Comment on the morphology of the erythrocytes.
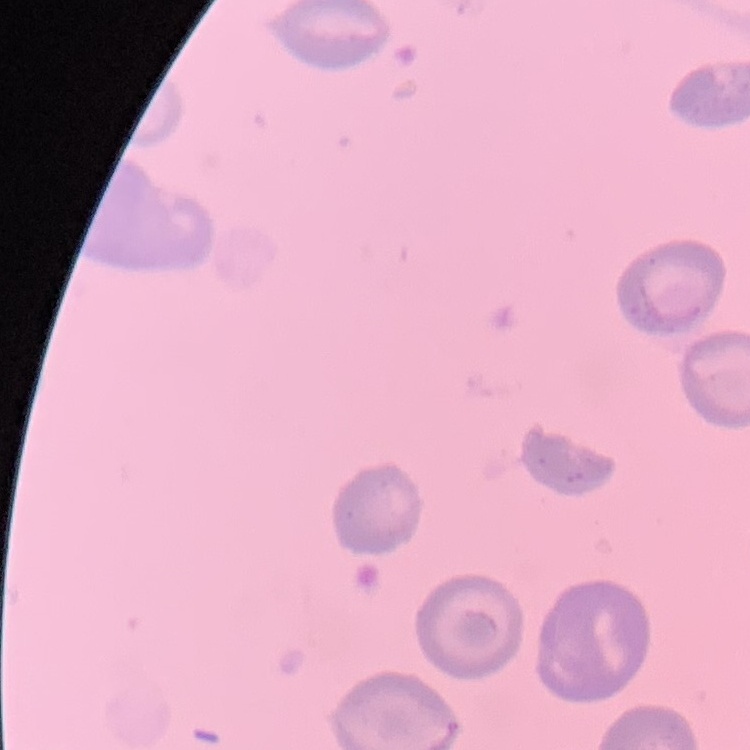

No rouleaux formation.

Stained with either Field's or Giemsa. Square crop of a larger photomicrograph. Thin peripheral smear.